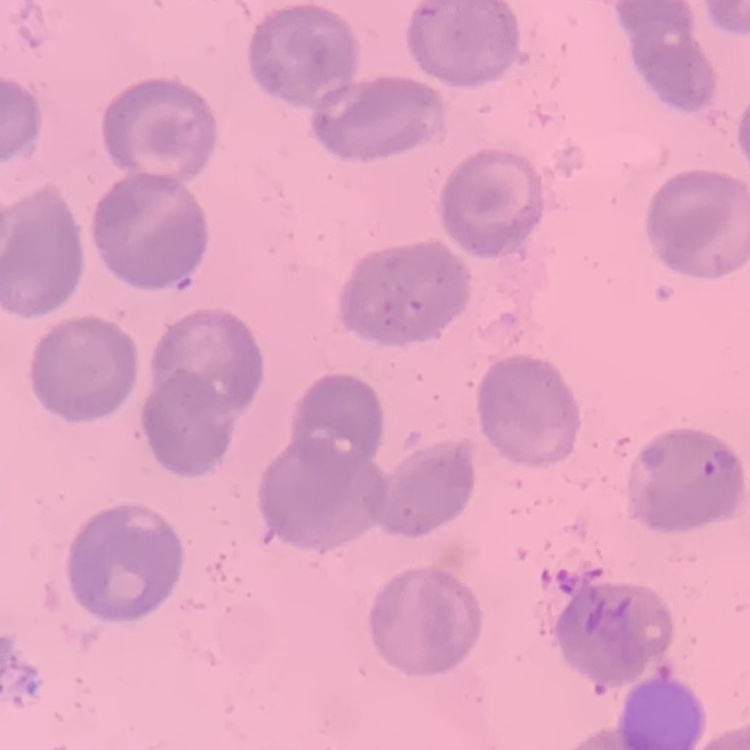
The erythrocytes show no rouleaux formation. Thin blood smear. Square crop of a larger photomicrograph. Field's or Giemsa stain.